Describe the morphology of the red blood cells.
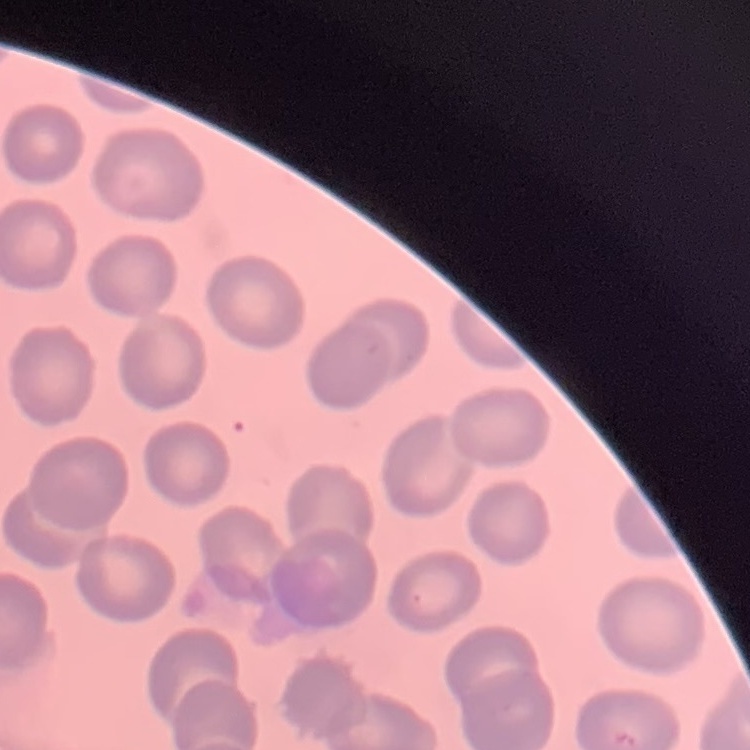
They show no rouleaux formation.

preparation = thin peripheral smear
stain = Field's or Giemsa
image type = one tile cut from a larger photomicrograph